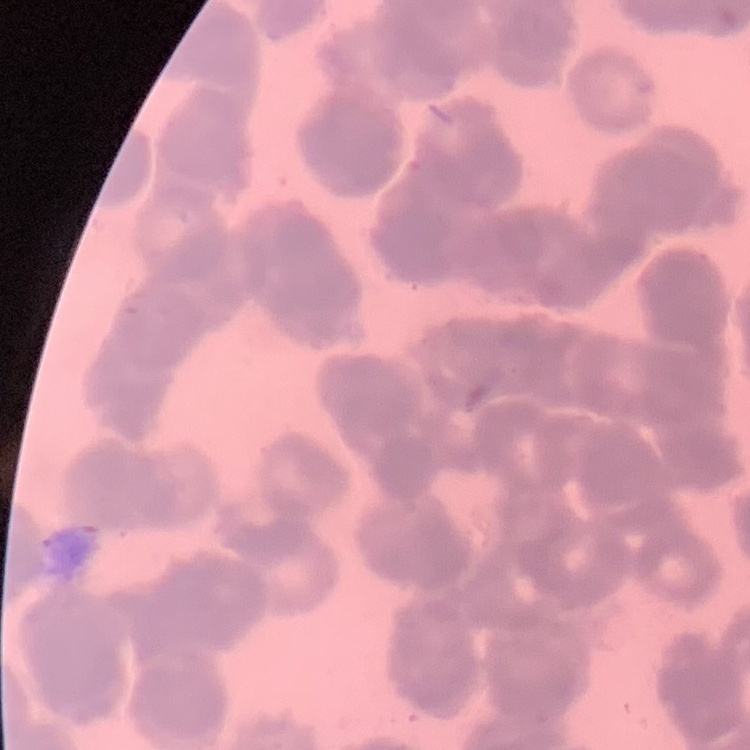
Summary:
  - Erythrocyte morphology: rouleaux formation
  - Stain: Field's or Giemsa
  - Image type: square crop of a larger photomicrograph
  - Preparation: thin peripheral smear